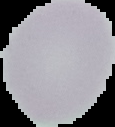
{
  "image_type": "segmented cell region on a black background",
  "image_size": "115×127 pixels",
  "preparation": "thin blood film",
  "result": "no Plasmodium parasites detected"
}